Report the malaria status of this cell.
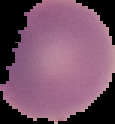
It is uninfected.

Image is 115×124 pixels. Cell region segmented out of the field of view; the surrounding area is masked to black. From a thin blood film.